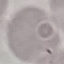

Result: no malaria parasites seen. Cell patch, automatically extracted from a larger field of view and resized to 64 × 64 pixels. Giemsa-stained preparation. Thin blood film. Photographed with a smartphone camera at the microscope eyepiece.